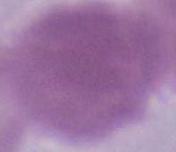 Captured at 1000x magnification. An erythrocyte is seen. Photomicrograph.